Assess for parasitized red blood cells.
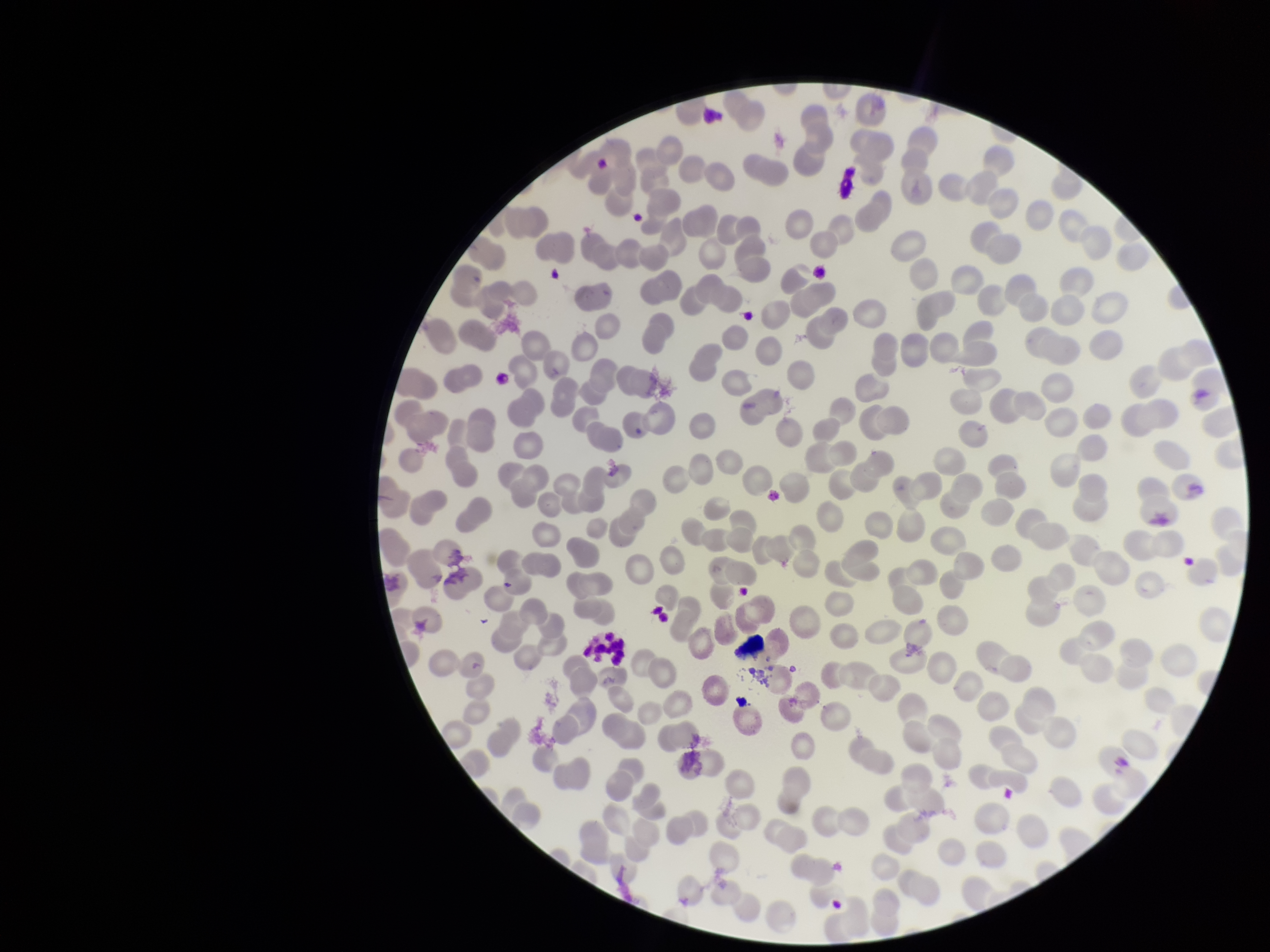

None seen.

Image is 1270×952 pixels. Giemsa stain. Red blood cell count: 239. Preparation: thin blood smear. Photographed through the microscope eyepiece with a smartphone camera. One field from this slide. Patient malaria status: negative. Parasitized red blood cell count: 0.